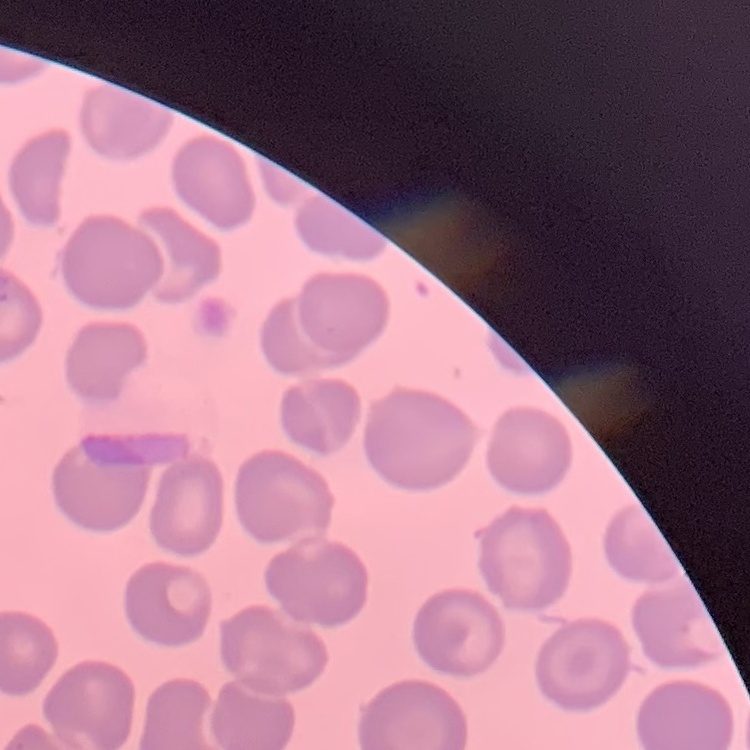 The erythrocytes show no rouleaux formation. One tile cut from a larger photomicrograph. Thin blood smear. Stained with either Field's or Giemsa.